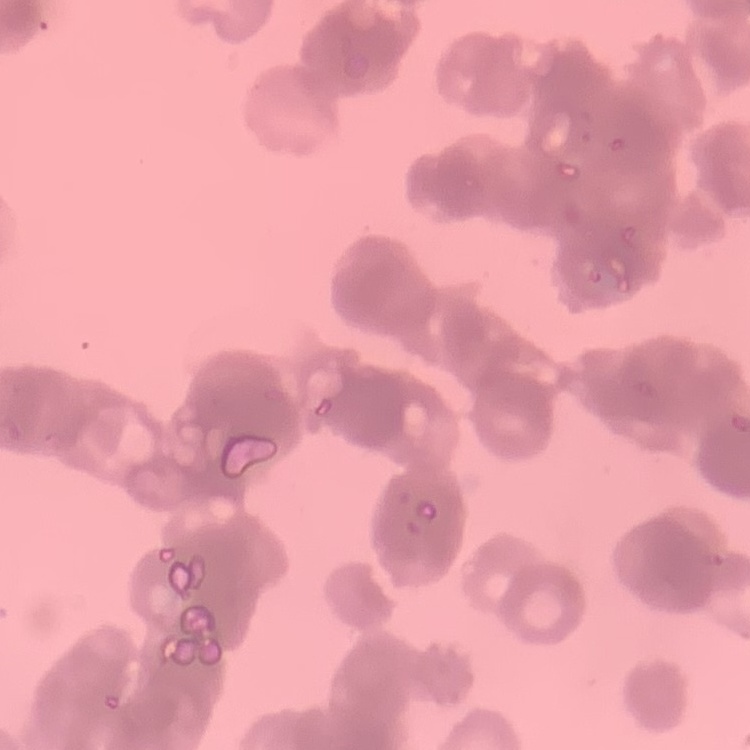
Summary:
  - Red blood cell morphology: rouleaux formation
  - Image type: square crop of a larger photomicrograph
  - Stain: Field's or Giemsa
  - Preparation: thin peripheral smear